Locate and identify every blood parasite.
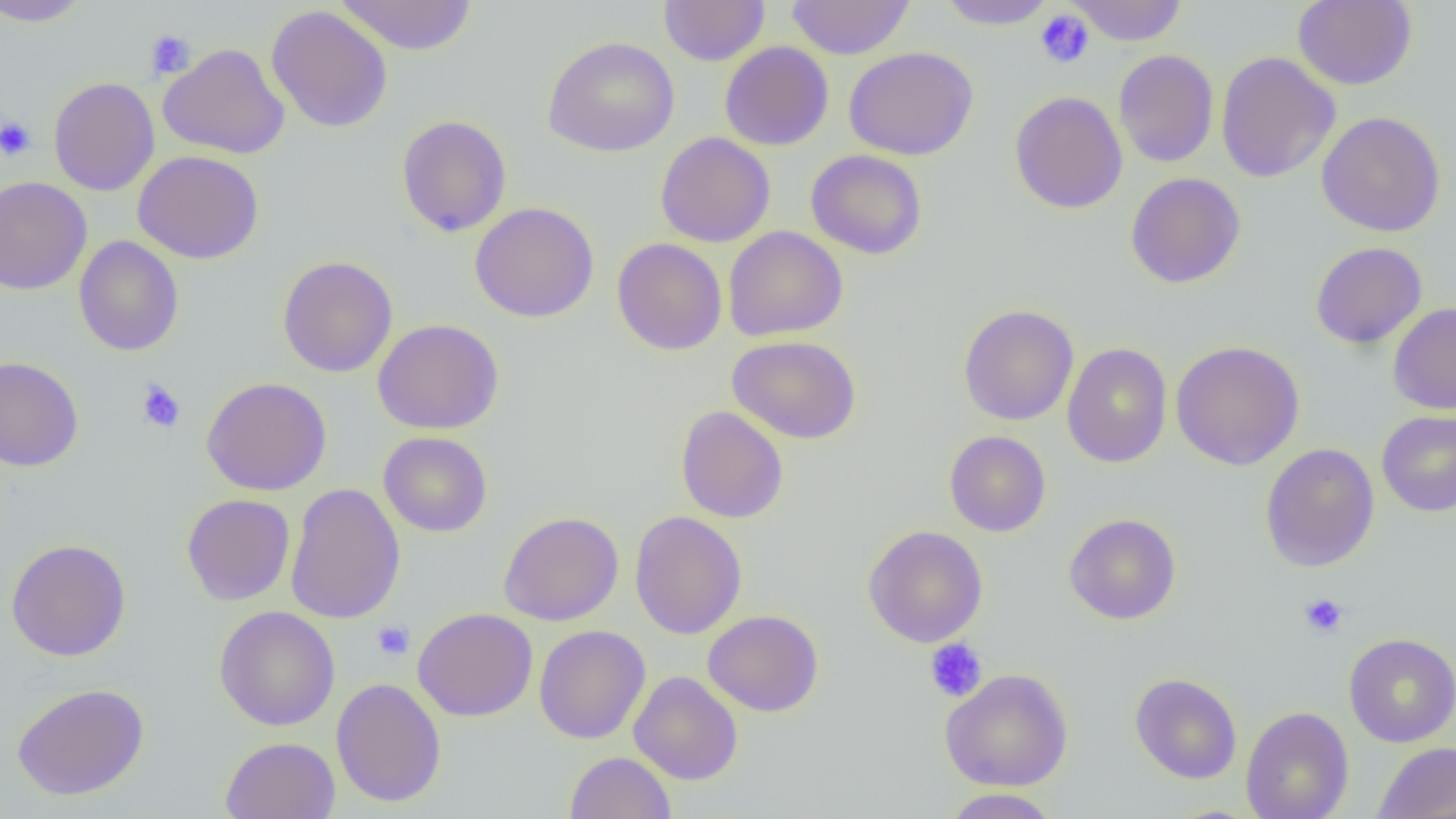
No blood parasites seen.

Summary:
  - Coordinate format: approximate bounding boxes as (x1,y1)-(x2,y2) corner pairs in pixels
  - Uninfected red blood cell locations: (0,0)-(92,27), (336,0)-(478,55), (658,0)-(770,66), (786,0)-(916,59), (1065,0)-(1188,45), (1293,0)-(1417,90), (935,1)-(1059,30), (266,5)-(393,133), (543,36)-(680,157), (719,41)-(834,151), (158,43)-(289,159), (844,46)-(978,160), (1113,49)-(1219,167), (1216,51)-(1340,183), (48,77)-(159,196), (1010,91)-(1128,214), (1317,111)-(1446,237), (395,114)-(512,237), (655,133)-(775,248), (806,149)-(928,259), (133,150)-(264,264), (1125,173)-(1246,288), (0,176)-(92,295), (470,202)-(600,323), (723,226)-(848,341), (74,235)-(184,356), (612,238)-(727,355), (1310,242)-(1427,348), (277,255)-(398,378), (1388,303)-(1456,415), (958,304)-(1079,425), (373,319)-(504,434), (728,335)-(861,443), (1170,340)-(1305,470), (1062,342)-(1173,468), (0,357)-(83,471), (201,377)-(332,496), (676,405)-(788,523), (1377,410)-(1456,517), (944,430)-(1051,537), (378,431)-(493,537), (1260,442)-(1380,572), (285,483)-(406,624), (181,493)-(295,606), (498,511)-(624,626), (629,511)-(747,640), (1064,513)-(1182,625), (862,525)-(988,648), (6,539)-(131,661), (214,606)-(340,730), (412,607)-(538,721), (703,610)-(823,716), (534,625)-(650,744), (1343,633)-(1456,747), (940,668)-(1074,791), (629,670)-(743,785), (1130,672)-(1243,784), (331,678)-(447,807), (11,683)-(149,801), (1240,706)-(1354,819), (221,736)-(340,819), (1373,741)-(1456,819), (565,751)-(676,819), (941,788)-(1061,818)
  - Platelet locations: (1034,9)-(1095,69), (145,29)-(197,79), (0,116)-(36,161), (136,380)-(185,432), (1299,592)-(1348,639), (372,620)-(415,661), (924,638)-(987,703)
  - Slide-level diagnosis: negative for blood parasites
  - Magnification: 1000x
  - Preparation: thin blood smear
  - Field of view: one of a larger specimen
  - Image size: 1456×819 pixels
  - Modality: optical microscopy